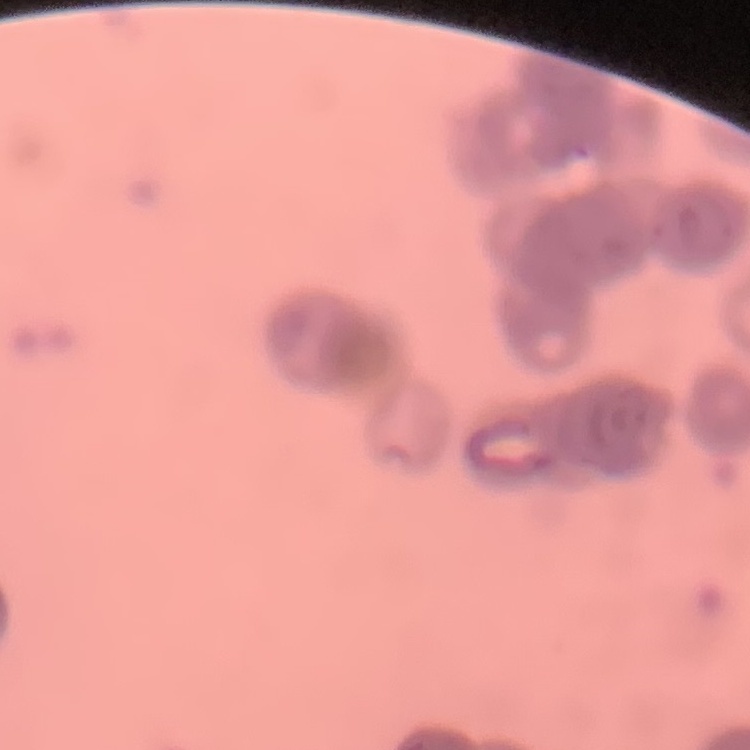

Summary:
  - Erythrocyte morphology: rouleaux formation
  - Preparation: thin blood film
  - Stain: Field's or Giemsa
  - Image type: one tile cut from a larger photomicrograph